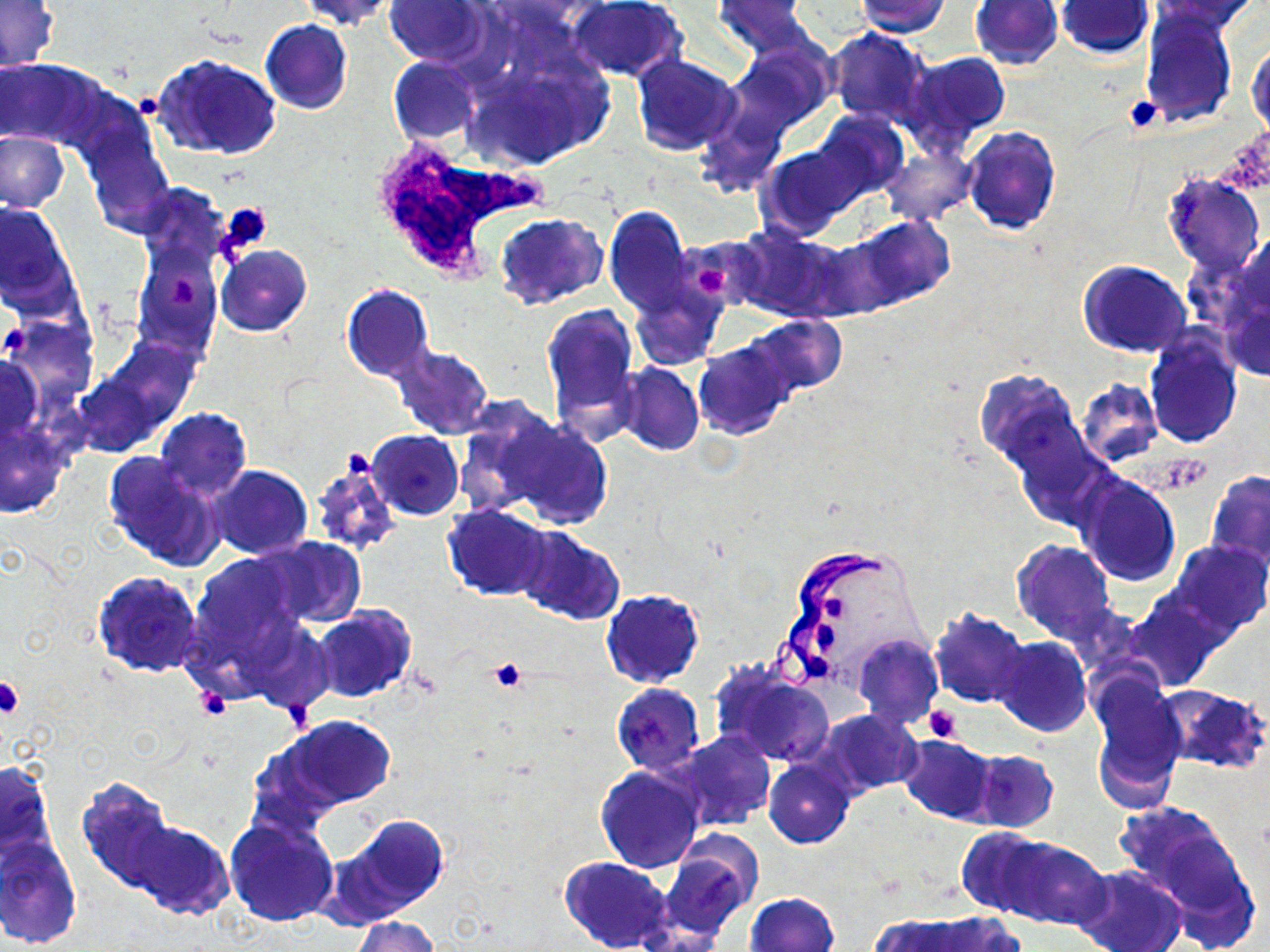

slide_level_diagnosis: Trypanosoma brucei
modality: optical microscopy
image_size: 1270×952 pixels
magnification: 1000x
uninfected_red_blood_cell_locations: 'approximate bounding boxes as named x1/y1/x2/y2 corners in pixels: (x1=298, y1=0, x2=397, y2=29), (x1=567, y1=0, x2=687, y2=83), (x1=711, y1=0, x2=815, y2=57), (x1=855, y1=0, x2=950, y2=37), (x1=1150, y1=0, x2=1260, y2=33), (x1=0, y1=1, x2=60, y2=71), (x1=385, y1=1, x2=489, y2=67), (x1=969, y1=1, x2=1063, y2=69), (x1=1057, y1=1, x2=1152, y2=58), (x1=1139, y1=8, x2=1236, y2=127), (x1=261, y1=20, x2=352, y2=115), (x1=826, y1=26, x2=933, y2=126), (x1=1248, y1=41, x2=1269, y2=137), (x1=460, y1=42, x2=611, y2=169), (x1=723, y1=43, x2=833, y2=141), (x1=901, y1=51, x2=1011, y2=151), (x1=152, y1=53, x2=282, y2=161), (x1=630, y1=54, x2=742, y2=156), (x1=388, y1=57, x2=480, y2=144), (x1=1, y1=58, x2=104, y2=149), (x1=815, y1=113, x2=907, y2=199), (x1=81, y1=126, x2=175, y2=237), (x1=962, y1=126, x2=1061, y2=235), (x1=0, y1=131, x2=69, y2=211), (x1=760, y1=143, x2=866, y2=236), (x1=882, y1=148, x2=974, y2=225), (x1=1163, y1=175, x2=1266, y2=275), (x1=0, y1=203, x2=75, y2=311), (x1=605, y1=204, x2=691, y2=317), (x1=496, y1=213, x2=605, y2=311), (x1=852, y1=216, x2=955, y2=311), (x1=734, y1=229, x2=843, y2=322), (x1=136, y1=231, x2=225, y2=359), (x1=679, y1=237, x2=764, y2=308), (x1=216, y1=245, x2=312, y2=336), (x1=1078, y1=260, x2=1192, y2=357), (x1=627, y1=274, x2=726, y2=371), (x1=341, y1=285, x2=433, y2=382), (x1=543, y1=303, x2=641, y2=444), (x1=745, y1=314, x2=848, y2=396), (x1=10, y1=321, x2=93, y2=401), (x1=1146, y1=331, x2=1242, y2=447), (x1=694, y1=342, x2=794, y2=439), (x1=388, y1=344, x2=493, y2=441), (x1=0, y1=355, x2=42, y2=442), (x1=617, y1=363, x2=703, y2=456), (x1=973, y1=369, x2=1080, y2=474), (x1=1076, y1=379, x2=1163, y2=466), (x1=459, y1=402, x2=583, y2=518), (x1=154, y1=407, x2=251, y2=501), (x1=503, y1=418, x2=612, y2=529), (x1=0, y1=427, x2=68, y2=519), (x1=368, y1=430, x2=464, y2=518), (x1=103, y1=452, x2=223, y2=571), (x1=307, y1=457, x2=400, y2=556), (x1=209, y1=465, x2=313, y2=559), (x1=1206, y1=470, x2=1270, y2=566), (x1=1076, y1=473, x2=1180, y2=585), (x1=442, y1=505, x2=551, y2=600), (x1=515, y1=526, x2=626, y2=625), (x1=254, y1=536, x2=366, y2=628), (x1=1012, y1=541, x2=1116, y2=644), (x1=1172, y1=541, x2=1270, y2=636), (x1=187, y1=553, x2=302, y2=672), (x1=92, y1=570, x2=205, y2=678), (x1=601, y1=589, x2=705, y2=687), (x1=1124, y1=595, x2=1223, y2=690), (x1=311, y1=607, x2=414, y2=703), (x1=928, y1=607, x2=1031, y2=710), (x1=247, y1=622, x2=337, y2=713), (x1=853, y1=635, x2=942, y2=729), (x1=993, y1=637, x2=1091, y2=737), (x1=712, y1=664, x2=835, y2=767), (x1=1088, y1=672, x2=1187, y2=808), (x1=611, y1=684, x2=705, y2=775), (x1=1157, y1=685, x2=1270, y2=773), (x1=819, y1=709, x2=921, y2=796), (x1=278, y1=716, x2=395, y2=813), (x1=671, y1=731, x2=776, y2=831), (x1=898, y1=734, x2=998, y2=825), (x1=968, y1=750, x2=1058, y2=833), (x1=1, y1=758, x2=57, y2=862), (x1=764, y1=758, x2=857, y2=848), (x1=595, y1=766, x2=705, y2=873), (x1=76, y1=775, x2=184, y2=896), (x1=1116, y1=801, x2=1241, y2=908), (x1=325, y1=813, x2=451, y2=926), (x1=122, y1=815, x2=234, y2=921), (x1=224, y1=817, x2=338, y2=928), (x1=956, y1=827, x2=1053, y2=919), (x1=660, y1=834, x2=762, y2=938), (x1=0, y1=836, x2=81, y2=949), (x1=997, y1=838, x2=1111, y2=930), (x1=560, y1=856, x2=674, y2=952), (x1=1074, y1=865, x2=1187, y2=952), (x1=744, y1=892, x2=839, y2=952), (x1=923, y1=914, x2=1023, y2=952), (x1=350, y1=916, x2=439, y2=952), (x1=873, y1=916, x2=969, y2=952)'
field_of_view: one of a larger specimen
stain: May-Grünwald-Giemsa
platelet_locations: 'approximate bounding boxes as named x1/y1/x2/y2 corners in pixels: (x1=1123, y1=95, x2=1165, y2=132), (x1=135, y1=98, x2=160, y2=116), (x1=219, y1=204, x2=273, y2=255), (x1=698, y1=266, x2=732, y2=299), (x1=168, y1=279, x2=197, y2=311), (x1=2, y1=321, x2=30, y2=357), (x1=822, y1=594, x2=846, y2=626), (x1=811, y1=625, x2=837, y2=652), (x1=488, y1=659, x2=527, y2=691), (x1=1, y1=678, x2=24, y2=719), (x1=195, y1=689, x2=232, y2=720), (x1=923, y1=705, x2=961, y2=743)'
preparation: thin blood film
trypanosoma_brucei_locations: 'approximate bounding boxes as named x1/y1/x2/y2 corners in pixels: (x1=773, y1=543, x2=893, y2=694)'
white_blood_cell_locations: 'approximate bounding boxes as named x1/y1/x2/y2 corners in pixels: (x1=359, y1=131, x2=549, y2=276)'